Locate every Plasmodium parasite.
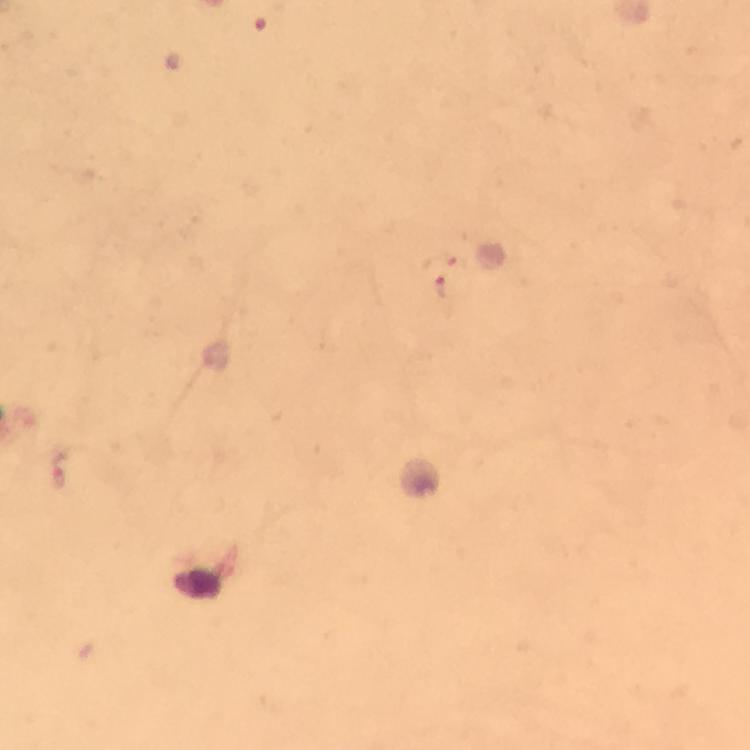
Approximate object centers, in pixels from the top-left corner.
Plasmodium parasites: (x=269, y=22), (x=444, y=280).

Summary:
  - Magnification: 100x
  - Image size: 750×750 pixels
  - Capture: smartphone mounted on the microscope
  - Context: from a malaria diagnostic workup
  - Immersion oil: used
  - Stain: Giemsa
  - Cropped from: a single field of view
  - Preparation: thick blood smear